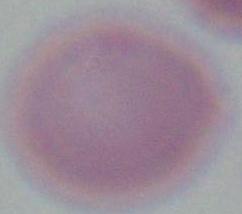

identification = red blood cell
modality = micrograph
magnification = 1000x